State which parasite is depicted.
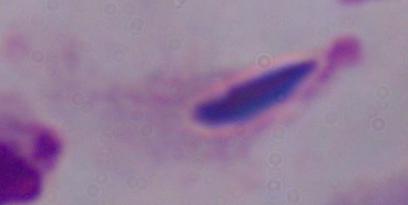
This is a trichomonad.

Summary:
  - Modality: photomicrograph
  - Magnification: 1000x